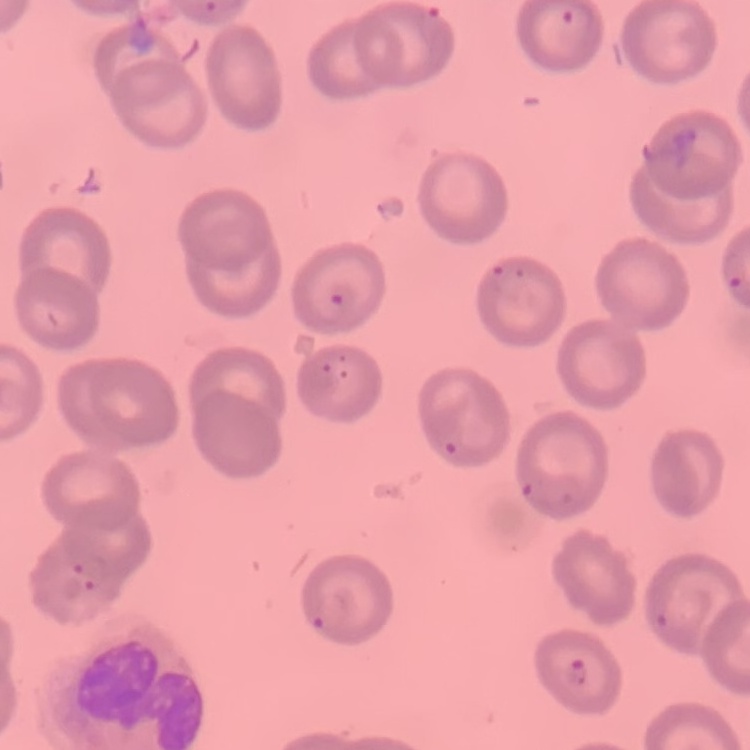
erythrocyte morphology = no rouleaux formation
preparation = thin blood film
image type = square crop of a larger photomicrograph
stain = Field's or Giemsa